Classify this cell by malaria status.
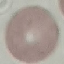
Uninfected.

capture = smartphone through the microscope eyepiece
image type = cell patch, automatically extracted from a larger field of view and resized to 64 × 64 pixels
stain = Giemsa
preparation = thin blood film